State the blood parasite species.
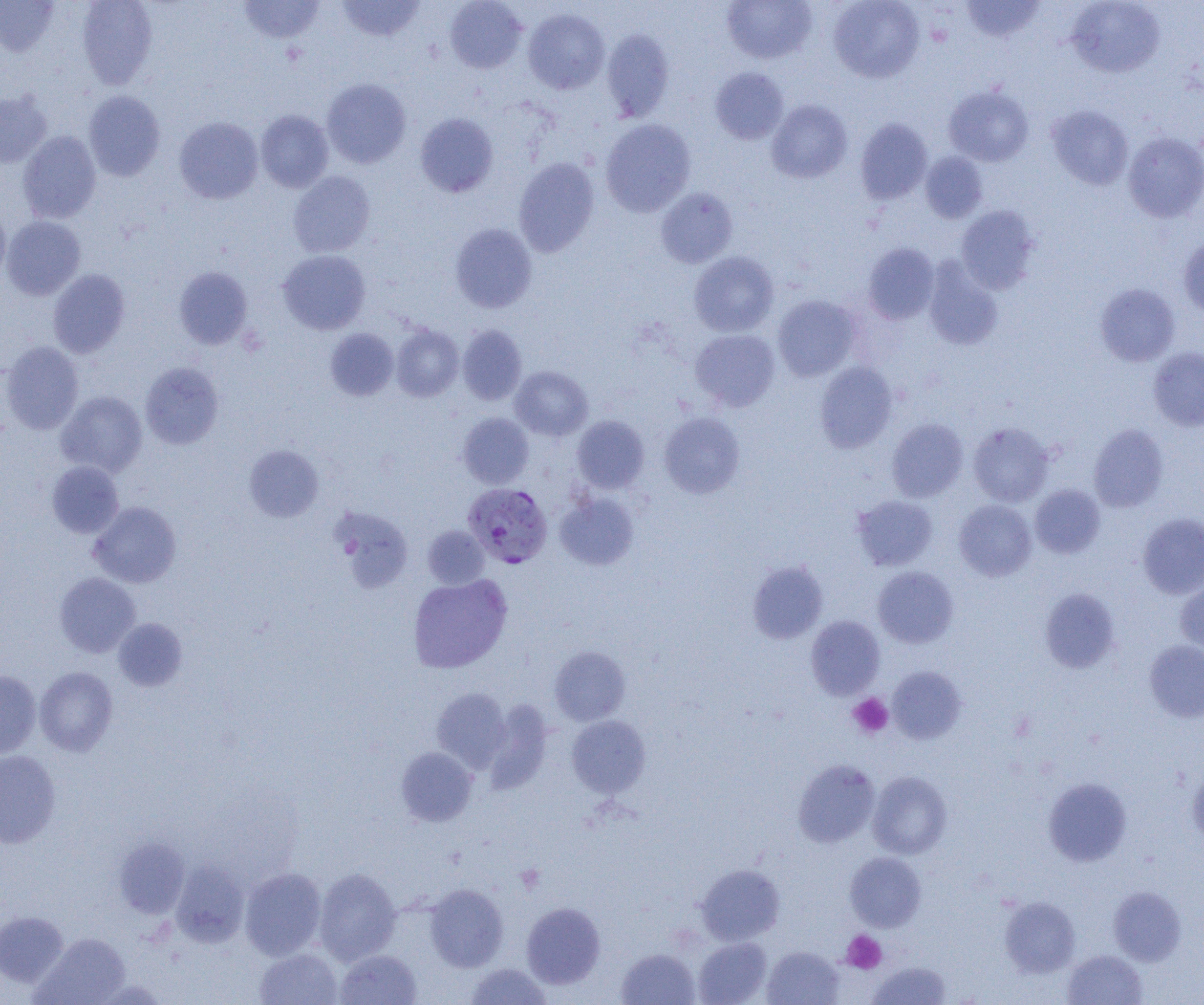
Plasmodium falciparum.

Approximate bounding boxes as named x1/y1/x2/y2 corners in pixels. Plasmodium falciparum-infected red blood cell locations: (x1=463, y1=483, x2=553, y2=568). Platelet locations: (x1=849, y1=693, x2=893, y2=738), (x1=516, y1=864, x2=545, y2=893), (x1=841, y1=930, x2=886, y2=974). Uninfected red blood cell locations: (x1=77, y1=0, x2=157, y2=89), (x1=239, y1=0, x2=325, y2=44), (x1=336, y1=0, x2=426, y2=42), (x1=444, y1=0, x2=527, y2=73), (x1=721, y1=0, x2=817, y2=64), (x1=828, y1=0, x2=924, y2=83), (x1=1067, y1=0, x2=1165, y2=77), (x1=0, y1=1, x2=59, y2=56), (x1=961, y1=1, x2=1045, y2=42), (x1=523, y1=9, x2=610, y2=94), (x1=601, y1=29, x2=674, y2=122), (x1=710, y1=67, x2=789, y2=144), (x1=321, y1=78, x2=411, y2=168), (x1=943, y1=86, x2=1033, y2=166), (x1=83, y1=91, x2=165, y2=181), (x1=0, y1=92, x2=52, y2=167), (x1=766, y1=99, x2=852, y2=183), (x1=1046, y1=105, x2=1134, y2=189), (x1=256, y1=110, x2=334, y2=192), (x1=415, y1=113, x2=498, y2=198), (x1=174, y1=117, x2=263, y2=204), (x1=855, y1=118, x2=932, y2=204), (x1=600, y1=119, x2=696, y2=217), (x1=18, y1=131, x2=101, y2=223), (x1=1123, y1=132, x2=1204, y2=222), (x1=920, y1=151, x2=989, y2=223), (x1=513, y1=156, x2=599, y2=258), (x1=288, y1=171, x2=375, y2=257), (x1=656, y1=187, x2=738, y2=268), (x1=956, y1=206, x2=1040, y2=293), (x1=0, y1=207, x2=11, y2=283), (x1=1, y1=216, x2=85, y2=300), (x1=450, y1=223, x2=537, y2=313), (x1=1179, y1=238, x2=1204, y2=319), (x1=863, y1=243, x2=939, y2=325), (x1=278, y1=250, x2=370, y2=334), (x1=689, y1=251, x2=779, y2=337), (x1=923, y1=259, x2=1003, y2=350), (x1=174, y1=266, x2=252, y2=349), (x1=48, y1=269, x2=130, y2=358), (x1=1095, y1=283, x2=1180, y2=366), (x1=772, y1=295, x2=862, y2=381), (x1=457, y1=324, x2=526, y2=405), (x1=391, y1=325, x2=464, y2=401), (x1=325, y1=328, x2=398, y2=400), (x1=690, y1=329, x2=780, y2=412), (x1=1, y1=341, x2=84, y2=434), (x1=1147, y1=346, x2=1204, y2=431), (x1=140, y1=362, x2=224, y2=449), (x1=815, y1=362, x2=898, y2=453), (x1=510, y1=366, x2=593, y2=441), (x1=56, y1=390, x2=147, y2=477), (x1=458, y1=412, x2=534, y2=488), (x1=659, y1=412, x2=745, y2=498), (x1=572, y1=415, x2=649, y2=494), (x1=887, y1=419, x2=968, y2=502), (x1=967, y1=422, x2=1054, y2=507), (x1=1088, y1=424, x2=1169, y2=512), (x1=243, y1=444, x2=324, y2=522), (x1=47, y1=460, x2=124, y2=538), (x1=1030, y1=484, x2=1105, y2=558), (x1=555, y1=492, x2=639, y2=570), (x1=851, y1=494, x2=938, y2=571), (x1=954, y1=500, x2=1036, y2=581), (x1=88, y1=501, x2=181, y2=588), (x1=330, y1=507, x2=413, y2=593), (x1=1137, y1=513, x2=1204, y2=599), (x1=422, y1=525, x2=490, y2=589), (x1=747, y1=560, x2=828, y2=643), (x1=872, y1=566, x2=959, y2=648), (x1=54, y1=573, x2=140, y2=657), (x1=408, y1=574, x2=512, y2=673), (x1=1175, y1=578, x2=1204, y2=654), (x1=1039, y1=588, x2=1120, y2=673), (x1=806, y1=615, x2=884, y2=699), (x1=113, y1=618, x2=187, y2=691), (x1=1144, y1=640, x2=1204, y2=722), (x1=549, y1=646, x2=631, y2=725), (x1=35, y1=666, x2=117, y2=756), (x1=888, y1=666, x2=967, y2=743), (x1=0, y1=670, x2=41, y2=758), (x1=431, y1=687, x2=511, y2=771), (x1=484, y1=700, x2=552, y2=793), (x1=567, y1=715, x2=651, y2=798), (x1=396, y1=747, x2=477, y2=826), (x1=0, y1=750, x2=60, y2=848), (x1=793, y1=759, x2=880, y2=848), (x1=1187, y1=764, x2=1204, y2=845), (x1=867, y1=771, x2=952, y2=859), (x1=1043, y1=778, x2=1132, y2=866), (x1=115, y1=836, x2=189, y2=918), (x1=845, y1=851, x2=926, y2=931), (x1=170, y1=859, x2=249, y2=947), (x1=696, y1=863, x2=785, y2=945), (x1=240, y1=867, x2=327, y2=960), (x1=314, y1=867, x2=401, y2=964), (x1=425, y1=884, x2=508, y2=971), (x1=1108, y1=886, x2=1186, y2=966), (x1=999, y1=896, x2=1080, y2=978), (x1=521, y1=902, x2=605, y2=988), (x1=0, y1=912, x2=68, y2=987), (x1=33, y1=933, x2=131, y2=1004), (x1=693, y1=937, x2=771, y2=1005), (x1=762, y1=946, x2=844, y2=1005), (x1=255, y1=948, x2=342, y2=1005), (x1=617, y1=948, x2=700, y2=1005), (x1=335, y1=949, x2=422, y2=1005), (x1=1062, y1=949, x2=1147, y2=1005), (x1=866, y1=961, x2=952, y2=1004), (x1=464, y1=962, x2=552, y2=1004). Image is 1204×1005 pixels. 1000x magnification. One field of a larger specimen. Light microscopy. Thin blood smear.